Assess the morphology of the red blood cells.
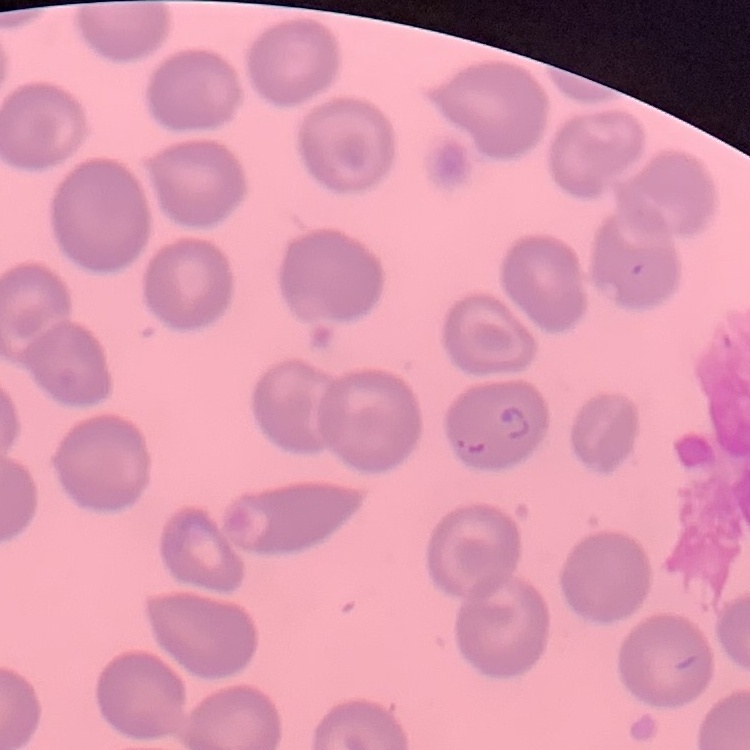
No rouleaux formation.

image type = one tile cut from a larger photomicrograph
preparation = thin blood film
stain = Field's or Giemsa